Assess the morphology of the erythrocytes.
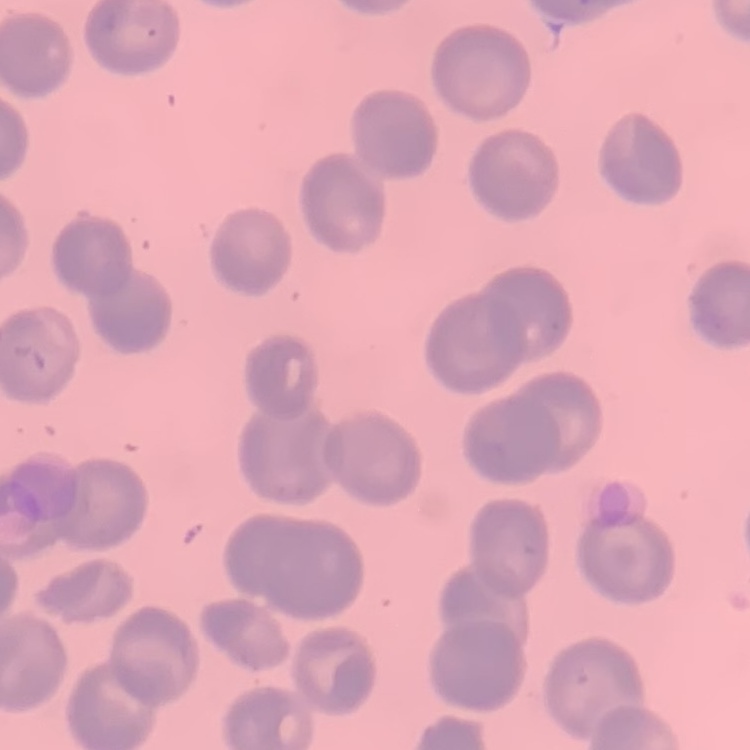

They show no rouleaux formation.

Summary:
  - Image type: one tile cut from a larger photomicrograph
  - Stain: Field's or Giemsa
  - Preparation: thin blood film